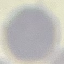
{
  "malaria_status": "uninfected",
  "preparation": "thin blood film",
  "stain": "Giemsa",
  "capture": "smartphone camera at the microscope eyepiece",
  "image_type": "cell patch, automatically extracted from a larger field of view and resized to 64 × 64 pixels"
}